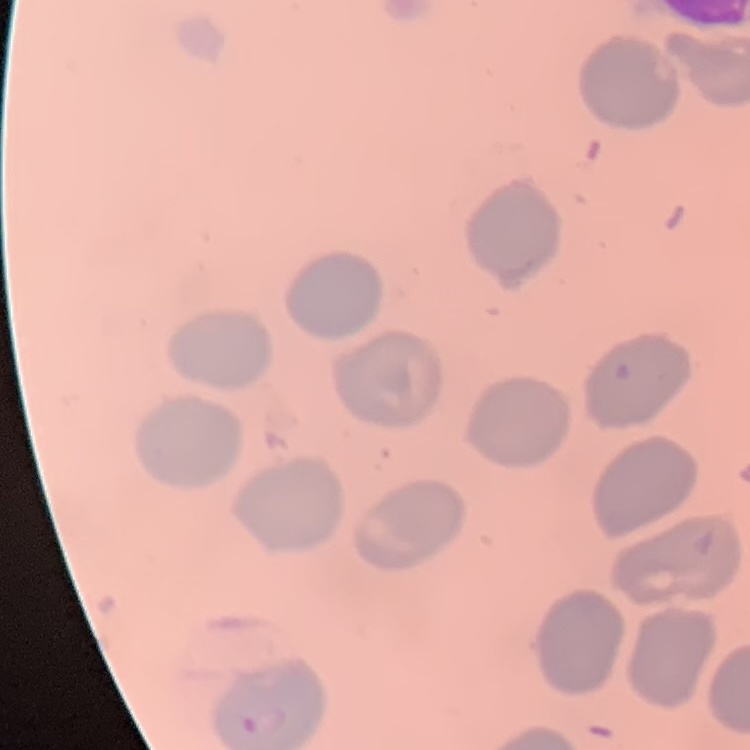

The erythrocytes exhibit no rouleaux formation. Thin blood smear. Field's or Giemsa stain. One tile cut from a larger photomicrograph.